Outline each Plasmodium falciparum-infected red blood cell.
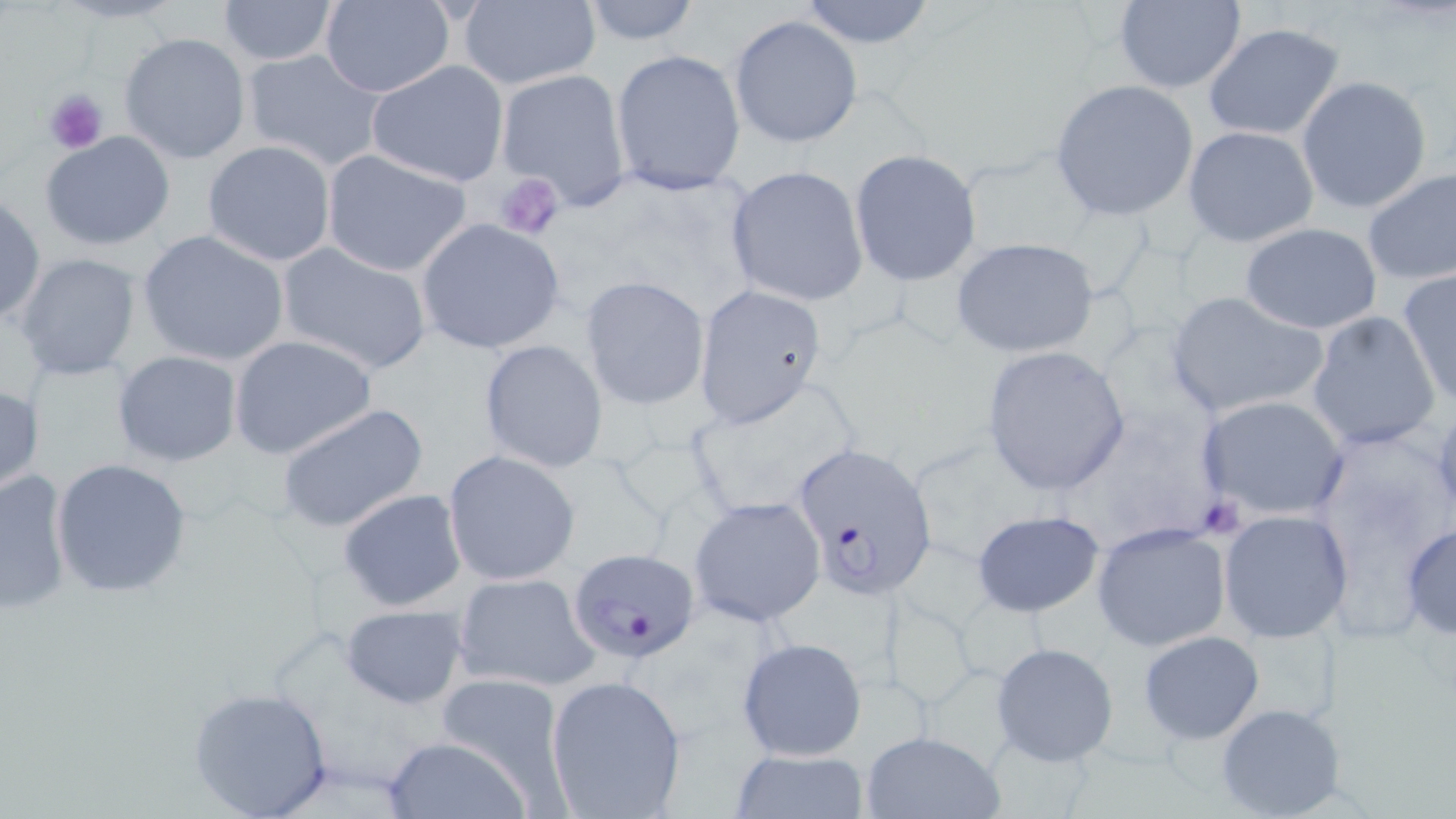

Approximate bounding boxes as named x1/y1/x2/y2 corners in pixels.
Plasmodium falciparum-infected red blood cells: (x1=790, y1=442, x2=940, y2=597), (x1=568, y1=546, x2=703, y2=664).

{
  "slide_level_diagnosis": "Plasmodium falciparum",
  "uninfected_red_blood_cell_locations": "approximate bounding boxes as named x1/y1/x2/y2 corners in pixels: (x1=575, y1=0, x2=703, y2=47), (x1=795, y1=0, x2=939, y2=49), (x1=215, y1=1, x2=341, y2=66), (x1=457, y1=1, x2=601, y2=90), (x1=1110, y1=1, x2=1248, y2=93), (x1=319, y1=2, x2=456, y2=97), (x1=728, y1=13, x2=864, y2=150), (x1=1201, y1=21, x2=1348, y2=141), (x1=118, y1=31, x2=252, y2=164), (x1=239, y1=48, x2=390, y2=172), (x1=611, y1=48, x2=747, y2=196), (x1=367, y1=59, x2=510, y2=188), (x1=495, y1=69, x2=631, y2=209), (x1=1296, y1=76, x2=1435, y2=215), (x1=1049, y1=79, x2=1201, y2=222), (x1=1181, y1=126, x2=1319, y2=247), (x1=41, y1=131, x2=176, y2=251), (x1=202, y1=140, x2=337, y2=266), (x1=320, y1=149, x2=474, y2=278), (x1=849, y1=150, x2=983, y2=288), (x1=723, y1=165, x2=869, y2=306), (x1=1360, y1=168, x2=1456, y2=286), (x1=0, y1=194, x2=46, y2=326), (x1=415, y1=219, x2=566, y2=354), (x1=1238, y1=221, x2=1383, y2=335), (x1=137, y1=229, x2=290, y2=367), (x1=950, y1=237, x2=1100, y2=359), (x1=276, y1=242, x2=433, y2=375), (x1=12, y1=251, x2=144, y2=382), (x1=1397, y1=271, x2=1456, y2=409), (x1=579, y1=275, x2=710, y2=410), (x1=691, y1=284, x2=826, y2=429), (x1=1164, y1=291, x2=1328, y2=421), (x1=1307, y1=311, x2=1440, y2=453), (x1=228, y1=335, x2=378, y2=460), (x1=478, y1=338, x2=609, y2=474), (x1=980, y1=345, x2=1133, y2=494), (x1=111, y1=349, x2=243, y2=467), (x1=684, y1=386, x2=863, y2=523), (x1=1195, y1=394, x2=1352, y2=524), (x1=278, y1=403, x2=429, y2=534), (x1=443, y1=450, x2=580, y2=586), (x1=50, y1=456, x2=193, y2=598), (x1=0, y1=468, x2=74, y2=614), (x1=336, y1=487, x2=468, y2=612), (x1=687, y1=496, x2=827, y2=628), (x1=1219, y1=509, x2=1353, y2=642), (x1=969, y1=510, x2=1106, y2=617), (x1=1090, y1=520, x2=1234, y2=652), (x1=1401, y1=521, x2=1456, y2=639), (x1=452, y1=571, x2=601, y2=692), (x1=340, y1=603, x2=469, y2=710), (x1=1138, y1=630, x2=1266, y2=744), (x1=735, y1=636, x2=868, y2=761), (x1=990, y1=640, x2=1121, y2=767), (x1=545, y1=672, x2=688, y2=819), (x1=431, y1=675, x2=571, y2=802), (x1=187, y1=684, x2=336, y2=819), (x1=1213, y1=702, x2=1347, y2=818), (x1=860, y1=730, x2=1003, y2=818), (x1=380, y1=733, x2=531, y2=818), (x1=729, y1=748, x2=870, y2=818)",
  "preparation": "thin blood smear",
  "stain": "May-Grünwald-Giemsa",
  "magnification": "1000x",
  "image_size": "1456×819 pixels",
  "platelet_locations": "approximate bounding boxes as named x1/y1/x2/y2 corners in pixels: (x1=44, y1=89, x2=107, y2=153), (x1=492, y1=172, x2=566, y2=242)",
  "modality": "light microscopy",
  "field_of_view": "one of a larger specimen"
}